Outline each blood parasite and name the species.
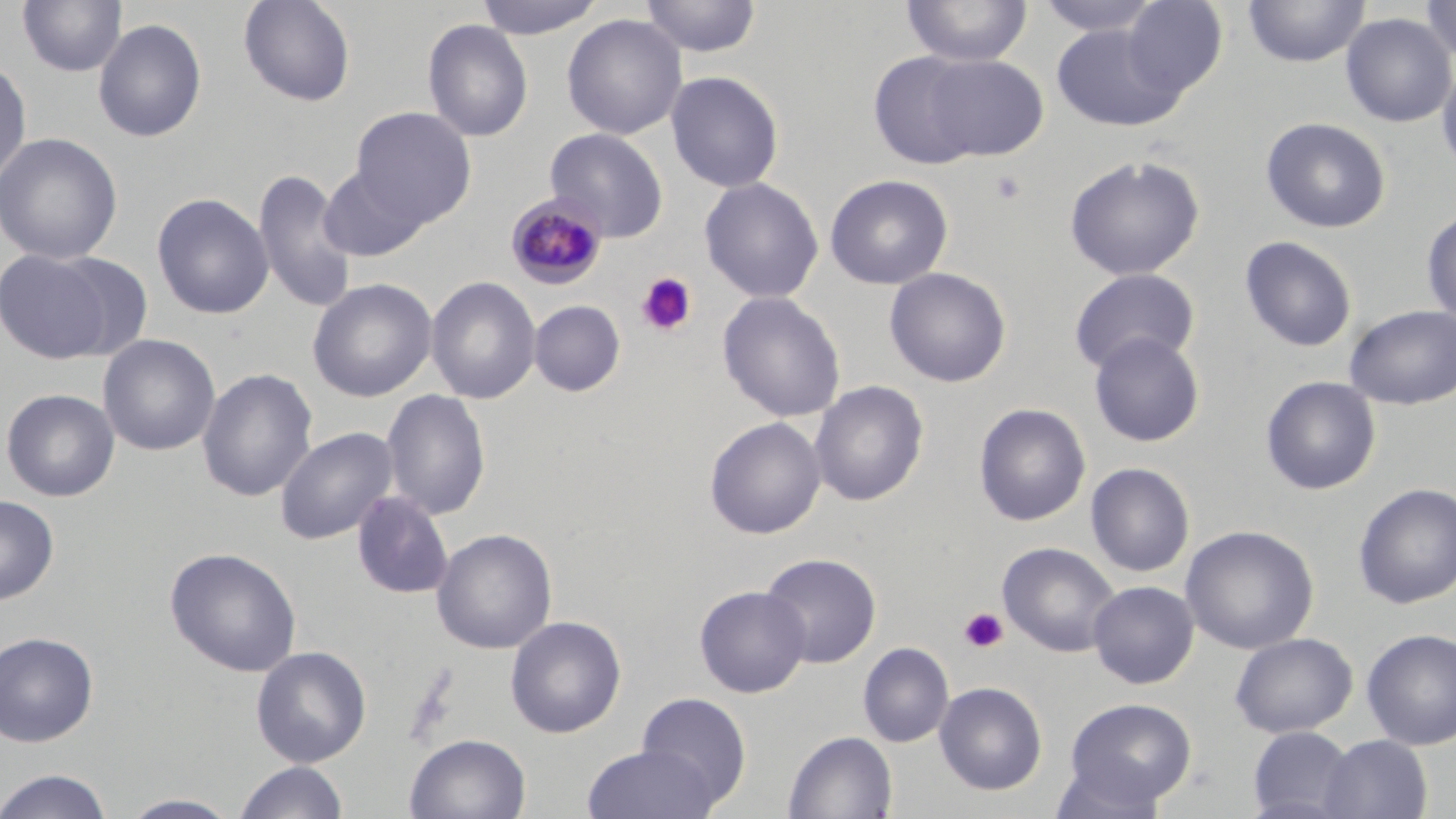
Approximate bounding boxes as named x1/y1/x2/y2 corners in pixels.
Plasmodium malariae-infected red blood cells: (x1=506, y1=194, x2=608, y2=289).
No Plasmodium falciparum, Plasmodium ovale, Plasmodium vivax, Babesia divergens, or Trypanosoma brucei observed.

Platelet locations: (x1=990, y1=169, x2=1028, y2=204), (x1=636, y1=272, x2=698, y2=337), (x1=958, y1=606, x2=1009, y2=654). Uninfected red blood cell locations: (x1=17, y1=0, x2=127, y2=78), (x1=238, y1=0, x2=356, y2=107), (x1=473, y1=0, x2=607, y2=39), (x1=639, y1=0, x2=762, y2=58), (x1=902, y1=0, x2=1033, y2=67), (x1=1034, y1=0, x2=1165, y2=37), (x1=1120, y1=0, x2=1227, y2=99), (x1=1242, y1=0, x2=1370, y2=68), (x1=1419, y1=0, x2=1456, y2=64), (x1=1340, y1=12, x2=1455, y2=127), (x1=561, y1=14, x2=688, y2=139), (x1=93, y1=18, x2=207, y2=143), (x1=423, y1=19, x2=533, y2=142), (x1=1051, y1=22, x2=1187, y2=131), (x1=867, y1=51, x2=988, y2=169), (x1=921, y1=55, x2=1049, y2=161), (x1=1436, y1=58, x2=1456, y2=176), (x1=0, y1=59, x2=32, y2=186), (x1=666, y1=70, x2=784, y2=193), (x1=350, y1=106, x2=477, y2=228), (x1=1261, y1=117, x2=1391, y2=233), (x1=545, y1=127, x2=669, y2=241), (x1=0, y1=132, x2=123, y2=265), (x1=1063, y1=154, x2=1205, y2=281), (x1=319, y1=165, x2=428, y2=262), (x1=253, y1=168, x2=358, y2=312), (x1=825, y1=174, x2=953, y2=290), (x1=699, y1=178, x2=824, y2=303), (x1=151, y1=192, x2=273, y2=319), (x1=1421, y1=207, x2=1456, y2=329), (x1=1240, y1=236, x2=1357, y2=352), (x1=0, y1=247, x2=118, y2=364), (x1=47, y1=253, x2=154, y2=360), (x1=884, y1=267, x2=1012, y2=388), (x1=1068, y1=268, x2=1200, y2=375), (x1=426, y1=276, x2=541, y2=404), (x1=307, y1=278, x2=437, y2=402), (x1=717, y1=292, x2=846, y2=423), (x1=529, y1=300, x2=625, y2=397), (x1=1344, y1=304, x2=1456, y2=410), (x1=1088, y1=332, x2=1205, y2=447), (x1=98, y1=334, x2=220, y2=456), (x1=196, y1=368, x2=318, y2=502), (x1=1260, y1=376, x2=1381, y2=495), (x1=809, y1=380, x2=929, y2=506), (x1=1, y1=388, x2=120, y2=502), (x1=380, y1=389, x2=491, y2=521), (x1=974, y1=403, x2=1091, y2=526), (x1=704, y1=416, x2=827, y2=539), (x1=274, y1=426, x2=399, y2=544), (x1=1085, y1=462, x2=1195, y2=578), (x1=1353, y1=482, x2=1456, y2=609), (x1=351, y1=490, x2=455, y2=600), (x1=0, y1=495, x2=59, y2=606), (x1=1181, y1=524, x2=1319, y2=655), (x1=431, y1=528, x2=557, y2=655), (x1=997, y1=542, x2=1121, y2=658), (x1=164, y1=547, x2=302, y2=677), (x1=759, y1=552, x2=881, y2=668), (x1=1087, y1=580, x2=1199, y2=688), (x1=694, y1=585, x2=811, y2=697), (x1=505, y1=615, x2=627, y2=738), (x1=1361, y1=627, x2=1456, y2=750), (x1=0, y1=631, x2=99, y2=746), (x1=1230, y1=632, x2=1357, y2=738), (x1=858, y1=642, x2=954, y2=747), (x1=250, y1=645, x2=371, y2=767), (x1=934, y1=681, x2=1048, y2=796), (x1=635, y1=691, x2=752, y2=808), (x1=1064, y1=697, x2=1197, y2=808), (x1=1247, y1=726, x2=1357, y2=818), (x1=784, y1=731, x2=898, y2=818), (x1=404, y1=733, x2=531, y2=819), (x1=1319, y1=735, x2=1432, y2=818), (x1=582, y1=744, x2=720, y2=819), (x1=233, y1=760, x2=348, y2=819), (x1=1050, y1=760, x2=1173, y2=819), (x1=0, y1=769, x2=115, y2=819), (x1=119, y1=793, x2=240, y2=818). Slide-level diagnosis: Plasmodium malariae. May-Grünwald-Giemsa-stained preparation. Thin blood smear. Captured at 1000x magnification. Optical microscopy. One field of a larger specimen. Image is 1456×819 pixels.